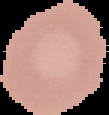

Summary:
  - Image type: cell region segmented out of the field of view; surrounding area masked to black
  - Malaria status: uninfected
  - Preparation: thin blood film
  - Image size: 109×115 pixels